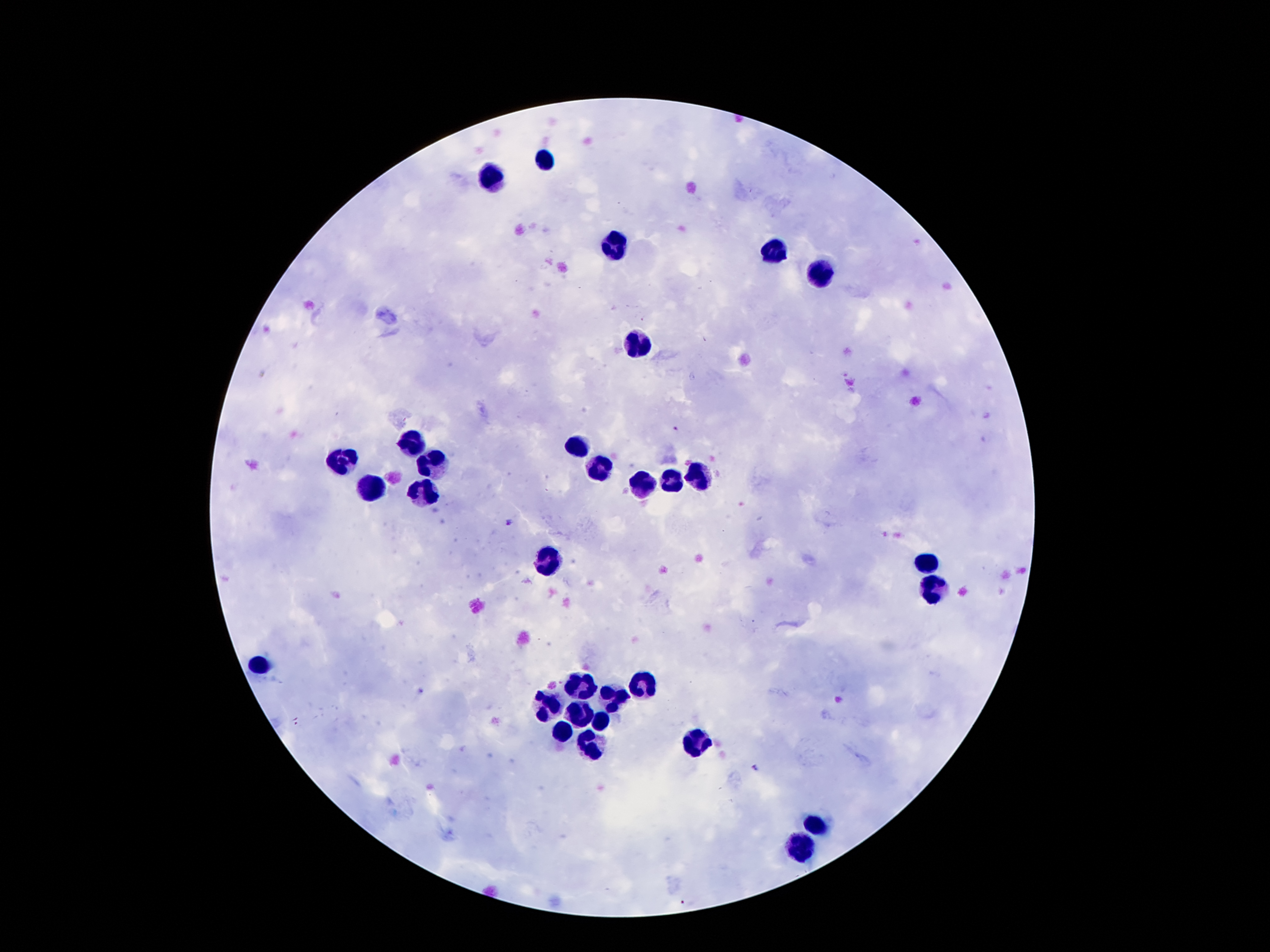
Approximate centers as {x, y} in pixels.
Summary:
  - Leukocyte locations: {544, 159}, {491, 178}, {615, 243}, {775, 253}, {821, 271}, {638, 344}, {409, 442}, {571, 446}, {340, 461}, {435, 462}, {596, 467}, {695, 474}, {670, 480}, {643, 484}, {372, 486}, {424, 493}, {550, 562}, {926, 564}, {932, 586}, {258, 664}, {580, 681}, {643, 683}, {613, 698}, {544, 704}, {577, 711}, {596, 721}, {561, 732}, {693, 740}, {590, 742}, {813, 822}, {800, 845}
  - Malaria parasite locations: {675, 430}, {508, 524}, {296, 722}, {757, 769}
  - Field of view: single
  - Patient malaria status: infected with Plasmodium falciparum
  - Capture: smartphone through the microscope eyepiece
  - Preparation: thick blood smear
  - Magnification: 100x
  - Stain: Giemsa
  - Image size: 1270×952 pixels